Look for parasitized red blood cells.
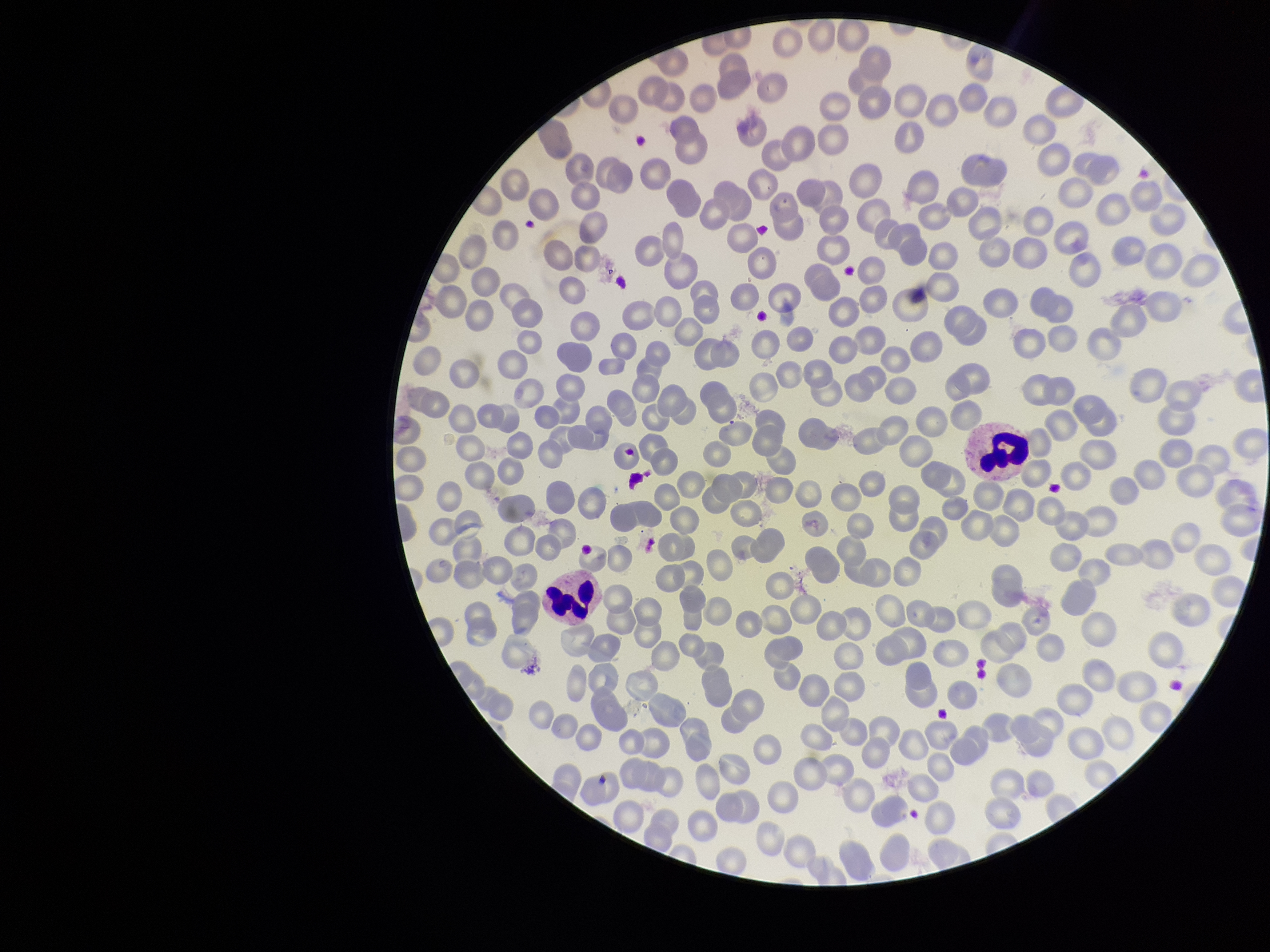

None seen.

{
  "stain": "Giemsa",
  "patient_malaria_status": "infected",
  "species_reported_for_this_patient": "Plasmodium falciparum",
  "preparation": "thin smear",
  "red_blood_cell_count": 265,
  "parasitized_red_blood_cell_count": 0,
  "image_size": "1270×952 pixels",
  "field_of_view": "one from this slide",
  "capture": "smartphone photograph through the microscope eyepiece"
}